Assess for Plasmodium parasites.
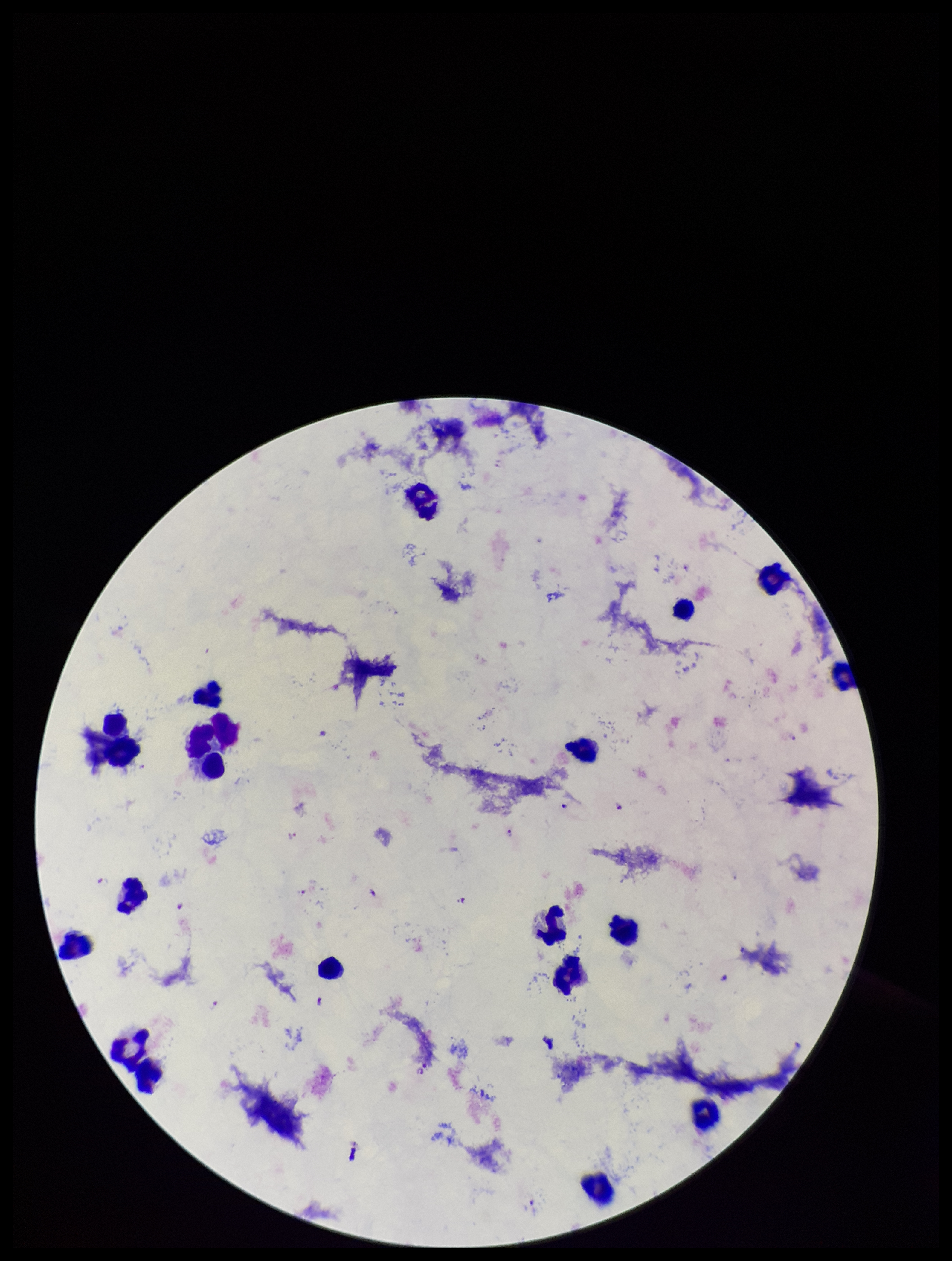
Detected.

Preparation: thick smear. Image is 952×1261 pixels. Stained with Giemsa. Species reported for this patient: Plasmodium falciparum. One field from this slide. Parasite count: 10. Smartphone photograph taken through the eyepiece of a microscope. Patient malaria status: positive. Leukocyte count: 20.